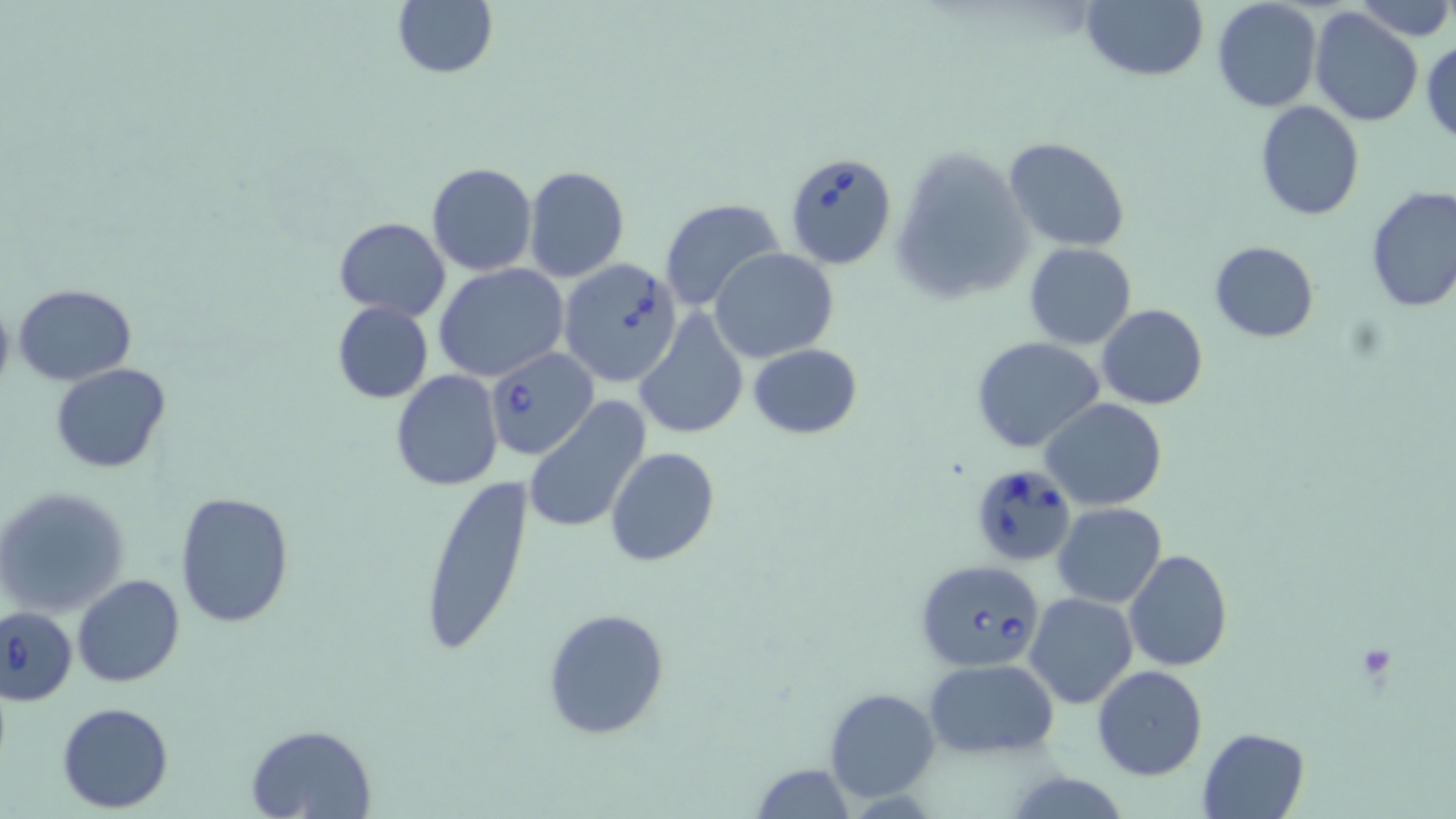

Summary:
  - Coordinate format: approximate bounding boxes as (x1,y1)-(x2,y2) corner pairs in pixels
  - Babesia divergens-infected red blood cell locations: (783,152)-(897,271), (558,257)-(683,386), (486,348)-(596,458), (966,463)-(1077,566), (915,558)-(1046,673), (0,606)-(78,706)
  - Uninfected red blood cell locations: (1080,0)-(1209,82), (1211,0)-(1323,113), (1348,0)-(1454,40), (391,1)-(497,79), (1309,6)-(1424,128), (1422,37)-(1455,146), (1255,102)-(1364,219), (1004,137)-(1131,253), (891,141)-(1034,304), (427,162)-(537,275), (523,165)-(629,282), (1364,186)-(1456,315), (660,198)-(785,314), (334,216)-(451,320), (1209,239)-(1318,344), (1024,242)-(1136,349), (710,248)-(839,362), (434,264)-(570,383), (14,285)-(137,385), (0,295)-(15,401), (332,301)-(434,404), (1097,303)-(1207,410), (633,308)-(749,440), (971,337)-(1106,454), (747,342)-(862,439), (52,363)-(171,474), (391,370)-(503,492), (524,397)-(653,535), (1041,398)-(1167,511), (605,448)-(720,565), (416,473)-(533,660), (1,488)-(129,616), (175,491)-(296,627), (1052,503)-(1168,607), (1122,549)-(1232,672), (72,574)-(185,688), (1025,593)-(1138,709), (542,608)-(671,740), (923,658)-(1059,759), (1092,665)-(1207,780), (825,688)-(940,803), (57,701)-(174,812), (247,724)-(375,818), (1197,727)-(1309,817), (751,763)-(856,817)
  - Slide-level diagnosis: Babesia divergens
  - Stain: May-Grünwald-Giemsa
  - Field of view: one of a larger specimen
  - Preparation: thin blood film
  - Magnification: 1000x
  - Image size: 1456×819 pixels
  - Modality: light microscopy